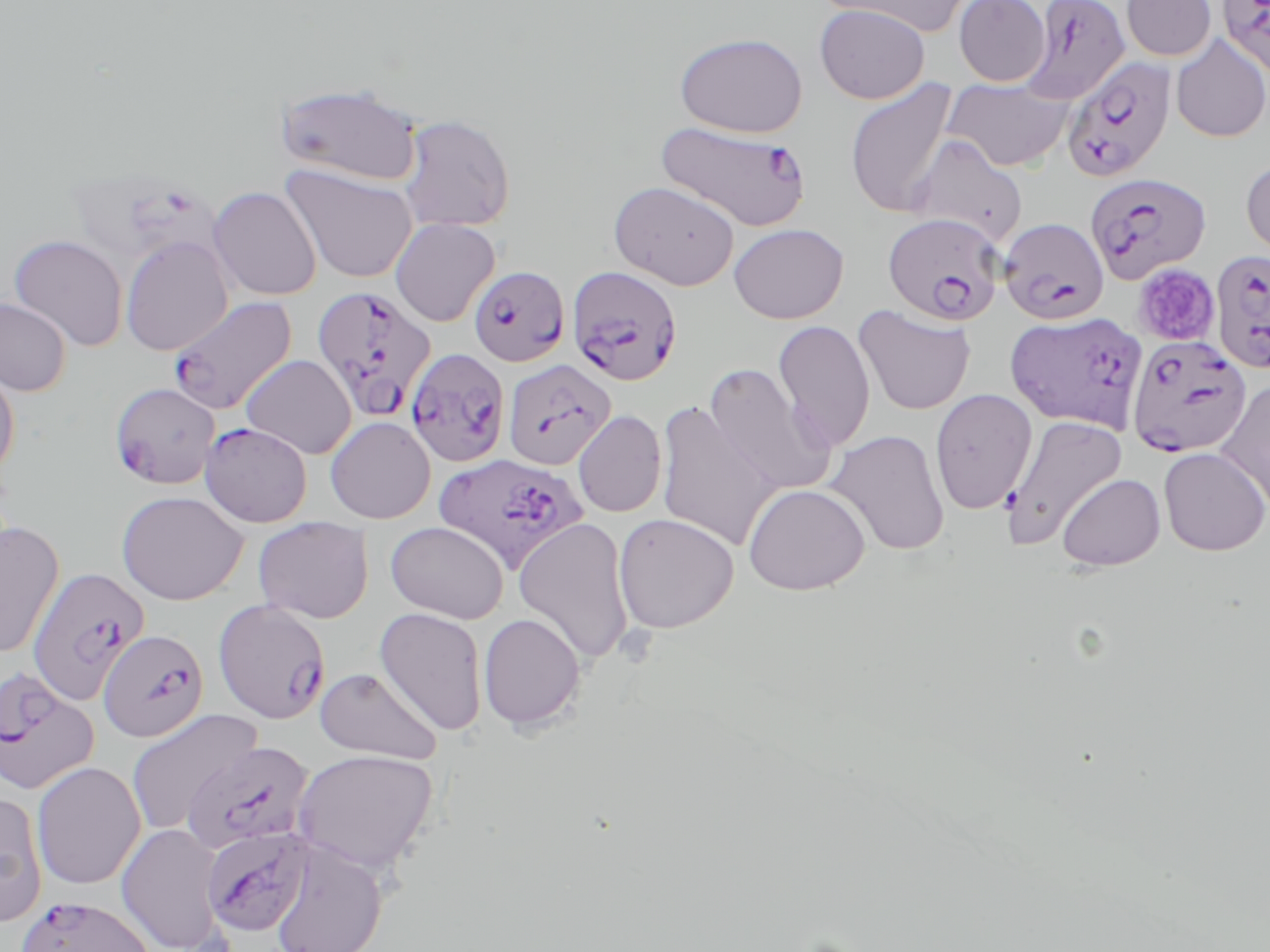 Approximate bounding boxes as named x1/y1/x2/y2 corners in pixels. Uninfected red blood cell locations (subset): (x1=821, y1=0, x2=972, y2=36), (x1=953, y1=0, x2=1050, y2=87), (x1=1122, y1=0, x2=1216, y2=61), (x1=814, y1=4, x2=930, y2=104), (x1=674, y1=32, x2=808, y2=138), (x1=1170, y1=35, x2=1270, y2=142), (x1=941, y1=76, x2=1076, y2=172), (x1=844, y1=78, x2=960, y2=218), (x1=275, y1=80, x2=425, y2=187), (x1=398, y1=114, x2=516, y2=232), (x1=906, y1=134, x2=1028, y2=248), (x1=1240, y1=157, x2=1270, y2=261), (x1=279, y1=164, x2=419, y2=284), (x1=609, y1=180, x2=740, y2=290), (x1=208, y1=186, x2=322, y2=300), (x1=390, y1=217, x2=500, y2=327), (x1=728, y1=223, x2=849, y2=324), (x1=9, y1=234, x2=129, y2=351), (x1=120, y1=236, x2=233, y2=356), (x1=0, y1=297, x2=71, y2=396), (x1=853, y1=304, x2=976, y2=415), (x1=772, y1=319, x2=876, y2=452), (x1=240, y1=354, x2=357, y2=459), (x1=0, y1=359, x2=20, y2=480), (x1=704, y1=363, x2=835, y2=496), (x1=1215, y1=379, x2=1270, y2=512), (x1=930, y1=389, x2=1037, y2=514), (x1=654, y1=399, x2=780, y2=552), (x1=573, y1=410, x2=667, y2=518), (x1=1001, y1=413, x2=1128, y2=549), (x1=325, y1=416, x2=435, y2=523), (x1=824, y1=429, x2=950, y2=556), (x1=1158, y1=447, x2=1269, y2=556), (x1=1056, y1=472, x2=1166, y2=571), (x1=743, y1=483, x2=870, y2=595), (x1=116, y1=490, x2=249, y2=606), (x1=614, y1=512, x2=740, y2=633), (x1=253, y1=516, x2=374, y2=623), (x1=513, y1=517, x2=635, y2=665), (x1=0, y1=521, x2=65, y2=660), (x1=385, y1=521, x2=509, y2=624), (x1=374, y1=606, x2=488, y2=736), (x1=478, y1=611, x2=586, y2=732), (x1=315, y1=666, x2=442, y2=764), (x1=125, y1=708, x2=262, y2=836), (x1=292, y1=748, x2=439, y2=876), (x1=31, y1=761, x2=146, y2=890), (x1=0, y1=790, x2=48, y2=927), (x1=116, y1=822, x2=228, y2=951), (x1=269, y1=839, x2=389, y2=952). Plasmodium falciparum-infected red blood cell locations (subset): (x1=1019, y1=0, x2=1131, y2=103), (x1=1216, y1=0, x2=1270, y2=78), (x1=1062, y1=56, x2=1176, y2=182), (x1=655, y1=120, x2=811, y2=232), (x1=1085, y1=170, x2=1212, y2=285), (x1=882, y1=213, x2=1006, y2=325), (x1=999, y1=217, x2=1110, y2=325), (x1=1209, y1=250, x2=1270, y2=374), (x1=468, y1=265, x2=569, y2=366), (x1=567, y1=265, x2=683, y2=386), (x1=311, y1=283, x2=437, y2=424), (x1=166, y1=295, x2=298, y2=415), (x1=1005, y1=311, x2=1148, y2=432), (x1=1127, y1=333, x2=1252, y2=457), (x1=405, y1=348, x2=510, y2=466), (x1=502, y1=358, x2=615, y2=470), (x1=109, y1=381, x2=221, y2=490), (x1=200, y1=422, x2=312, y2=528), (x1=433, y1=452, x2=587, y2=573), (x1=27, y1=567, x2=149, y2=704), (x1=213, y1=599, x2=331, y2=724), (x1=98, y1=628, x2=209, y2=742), (x1=183, y1=739, x2=314, y2=855), (x1=201, y1=825, x2=315, y2=938), (x1=15, y1=894, x2=157, y2=952). Platelet locations: (x1=1133, y1=263, x2=1220, y2=346). Slide-level diagnosis: Plasmodium falciparum. 1000x magnification. Thin blood film. Light microscopy. May-Grünwald-Giemsa stain. Image is 1270×952 pixels. Single field of view.